Report the malaria status of this cell.
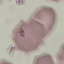
It is uninfected.

Thin blood smear. Cell patch, automatically extracted from a larger field of view and resized to 64 × 64 pixels. Photographed with a smartphone camera at the microscope eyepiece. Giemsa-stained preparation.